Classify this cell by malaria status.
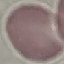
Uninfected.

Summary:
  - Preparation: thin smear
  - Stain: Giemsa
  - Image type: automatically extracted cell patch, resized to 64 × 64 pixels
  - Capture: smartphone camera at the microscope eyepiece